Assess this cell for malaria.
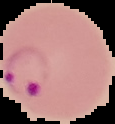
It is parasitized.

image type = segmented cell region on a black background
image size = 115×124 pixels
preparation = thin blood smear